Report the malaria status of this cell.
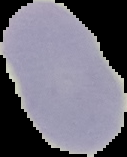

It is uninfected.

The area outside the segmented cell region is set to black. Image is 127×157 pixels. From a thin blood smear.